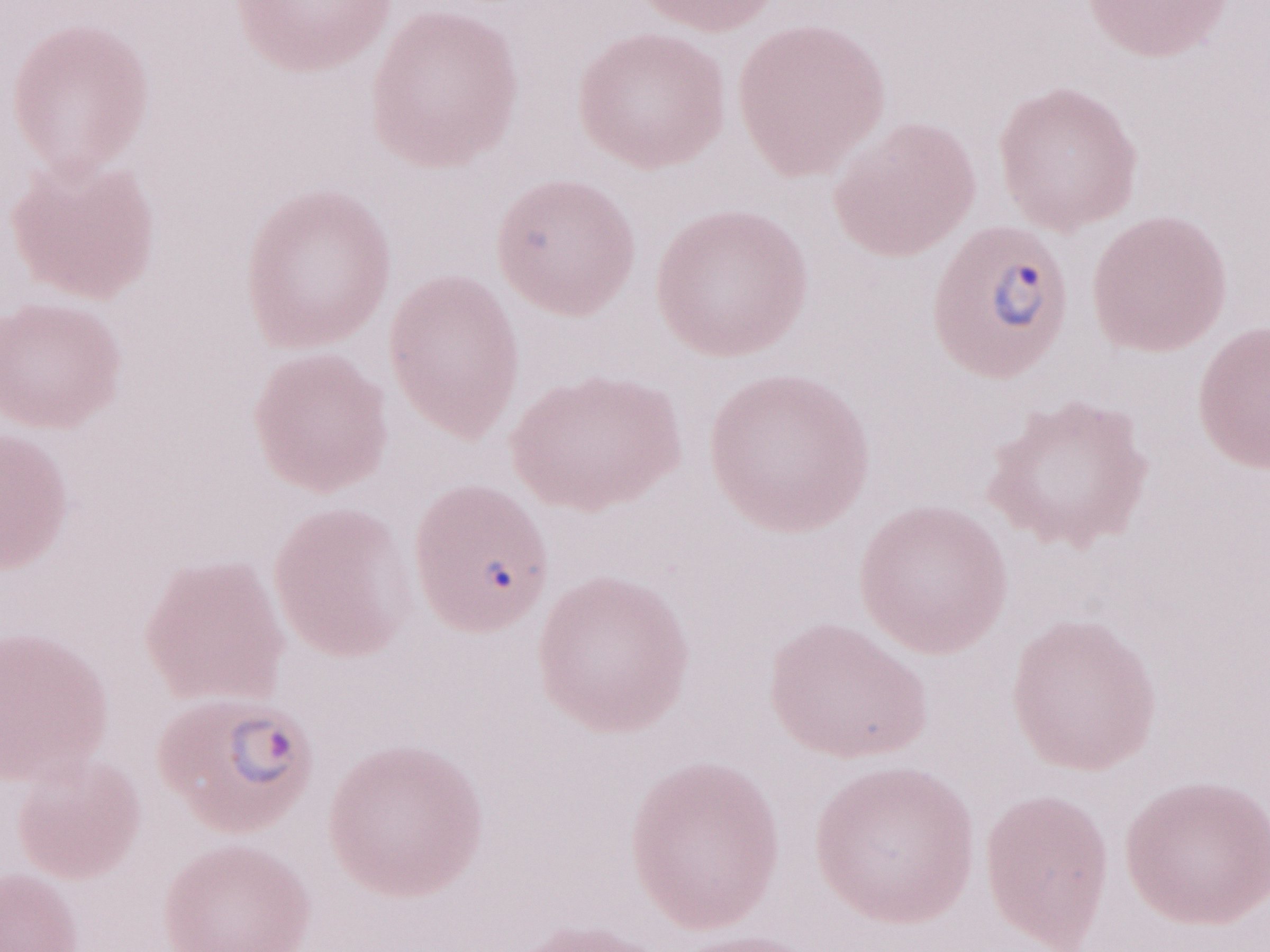

1,000x magnification. Thin peripheral-blood smear. Olympus BX43 microscope, Olympus DP73 camera. Image is 1270×952 pixels. Patient-level malaria diagnosis: positive. Single field of view. May-Grünwald-Giemsa stain.